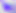
modality = micrograph
magnification = 400x
identification = Toxoplasma gondii